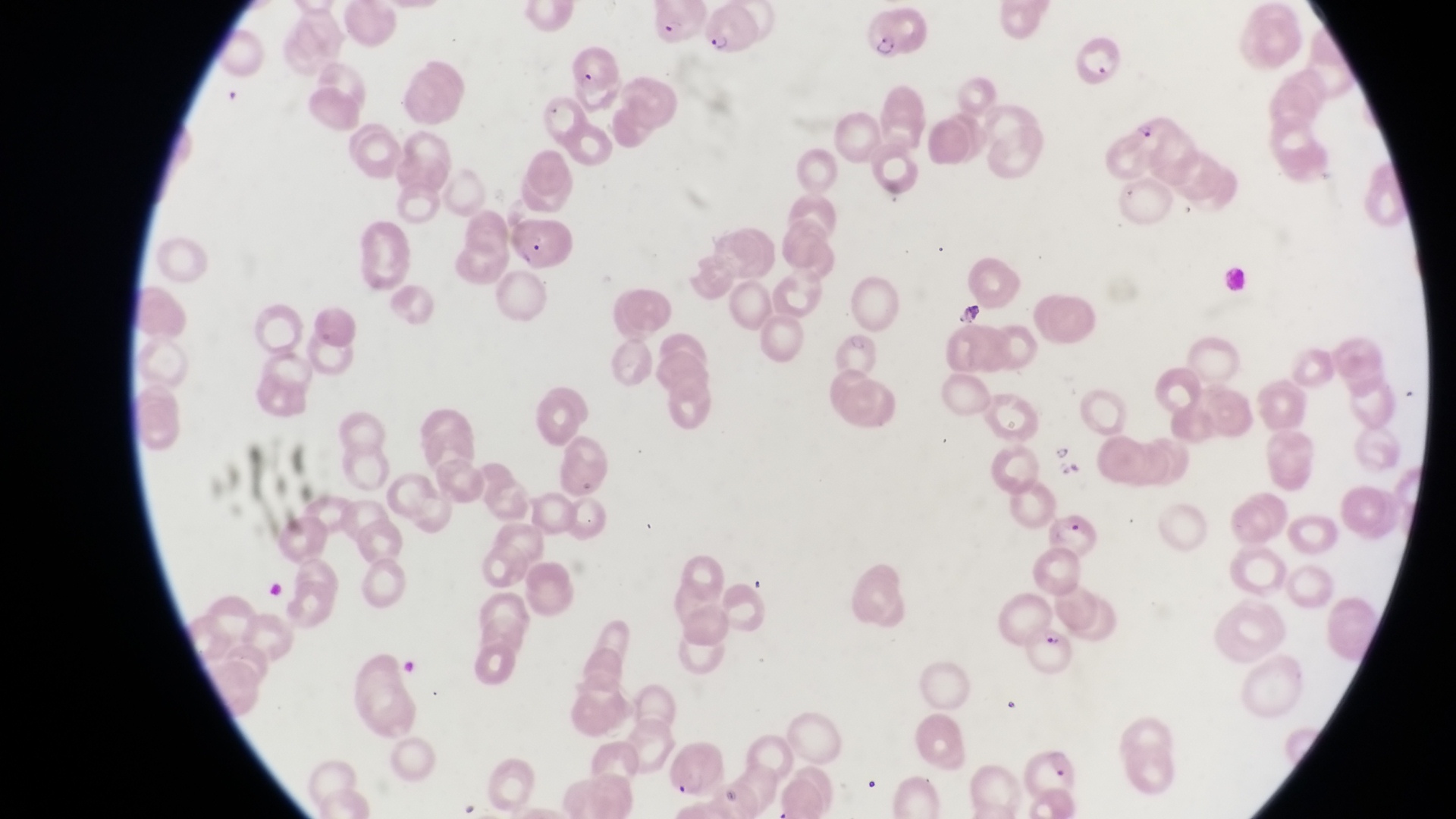
Approximate bounding boxes as {left, top, right, bottom} in pixels. Parasitised red blood cell locations: {855, 3, 919, 56}, {648, 5, 700, 50}, {703, 10, 761, 62}, {1079, 32, 1125, 86}, {1126, 108, 1181, 175}, {1037, 508, 1097, 560}, {1025, 621, 1081, 670}, {1018, 745, 1079, 805}. Artifact (platelet-like body, stain precipitate, or debris) locations: {954, 296, 986, 330}. Trophozoite locations: {1050, 439, 1077, 472}. Image is 1456×819 pixels. One field of view. At a magnification of 1000x. Collected in Uganda. Thin blood smear. Photographed through the eyepiece of an Olympus CX-23 microscope with a smartphone camera.